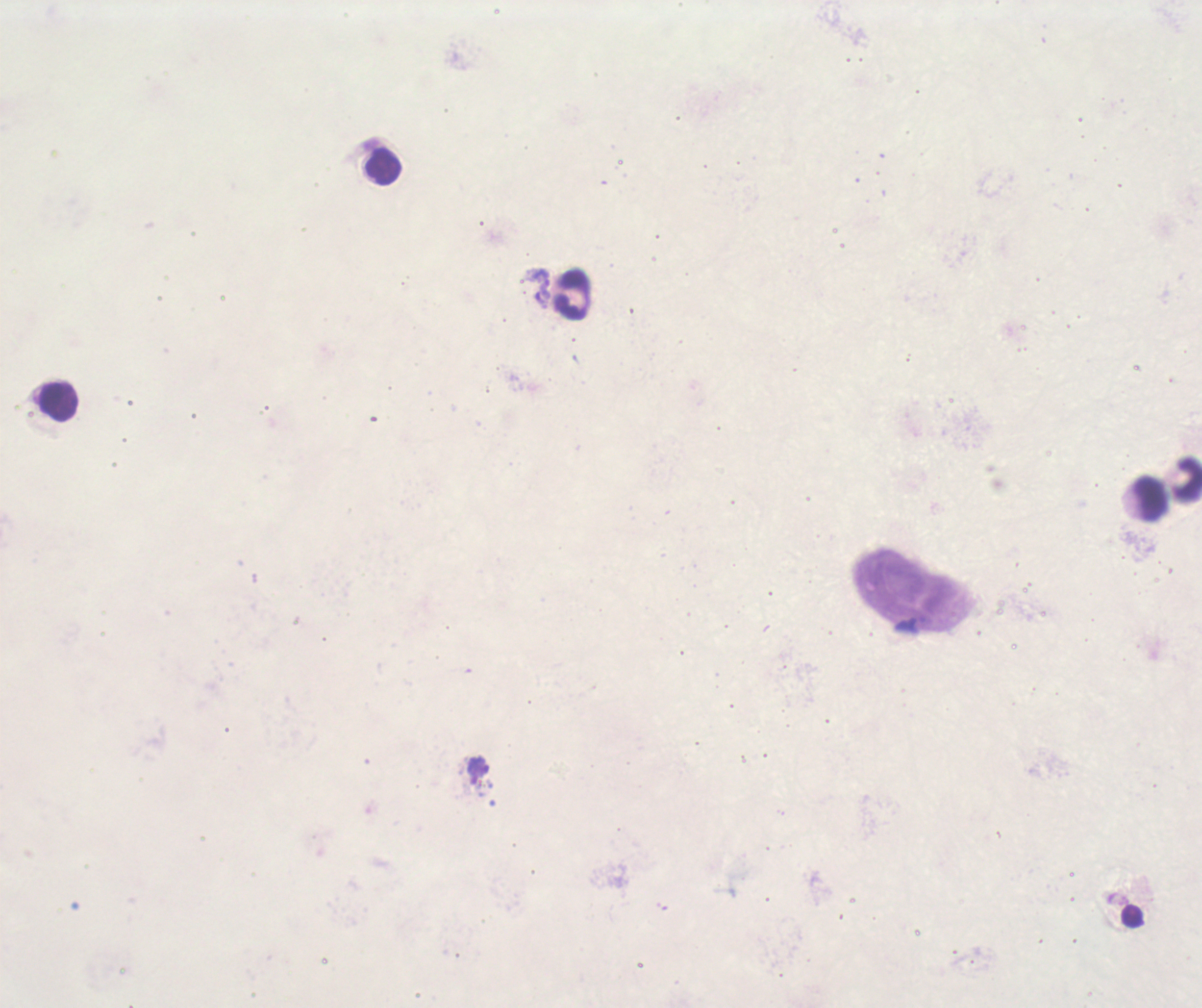 Approximate object centers, in pixels from the top-left corner. Trophozoite locations: (x=538, y=286), (x=478, y=767). Leukocyte locations: (x=382, y=166), (x=573, y=295), (x=56, y=404), (x=1187, y=478), (x=1148, y=499). One field from this slide. Background quality: poor. Thick blood film. 100x magnification. Image is 1202×1008 pixels. Coloration quality: bad. Previously used in a real diagnosis. Result: malaria parasites identified. Romanowsky stain.